Classify this cell by malaria status.
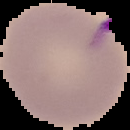

Parasitized.

The area outside the segmented cell region is set to black. From a thin blood film. Image is 130×130 pixels.